State the preparation type.
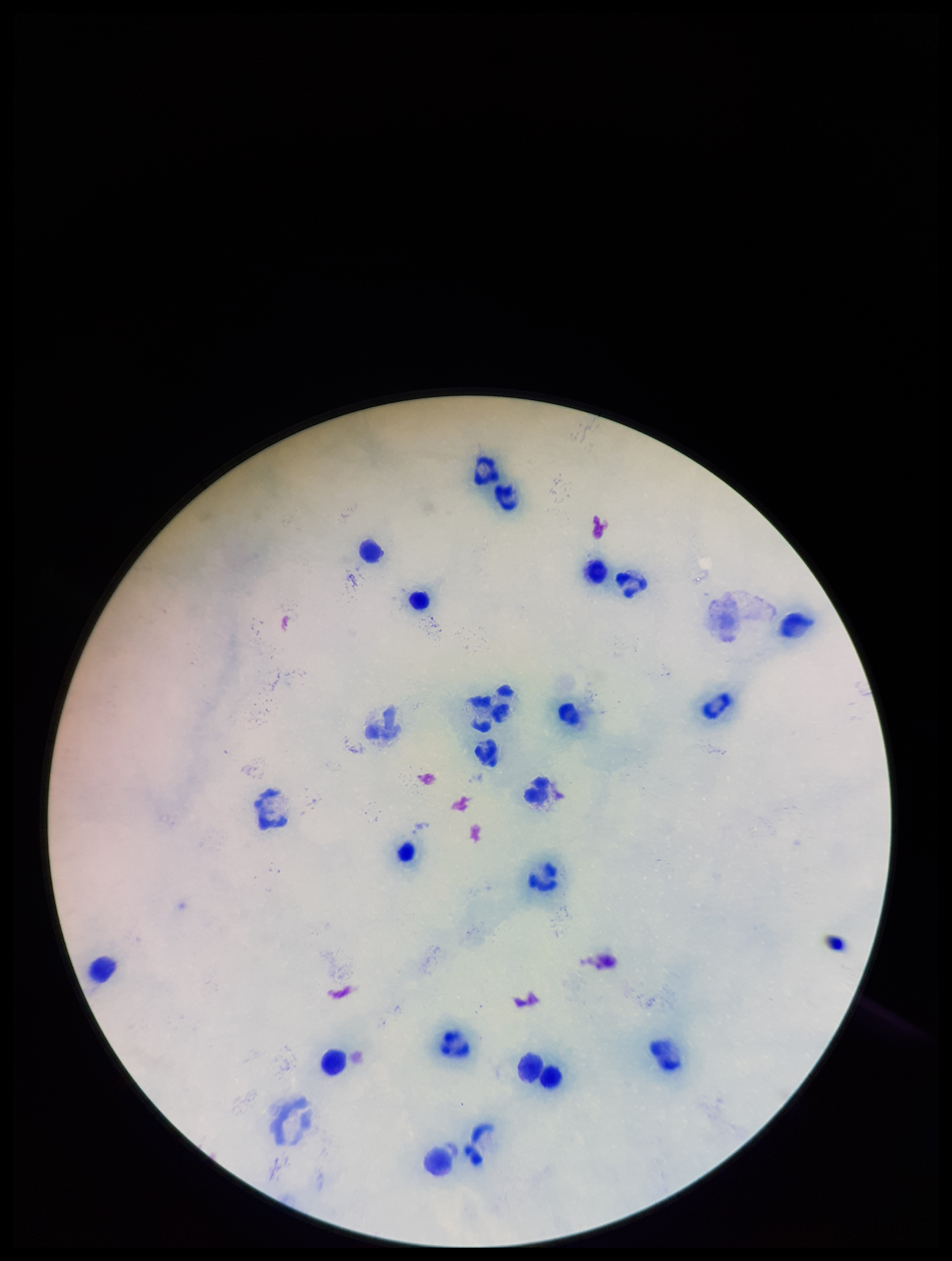

It is a thick blood smear.

Summary:
  - Plasmodium parasites: none seen
  - Capture: smartphone photograph through the microscope eyepiece
  - Patient malaria status: negative
  - Stain: Giemsa
  - Leukocyte count: 23
  - Field of view: one from this slide
  - Image size: 952×1261 pixels
  - Parasite count: 0